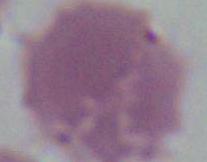

Captured at 1000x magnification. A red blood cell is seen. Micrograph.